Outline each uninfected red blood cell.
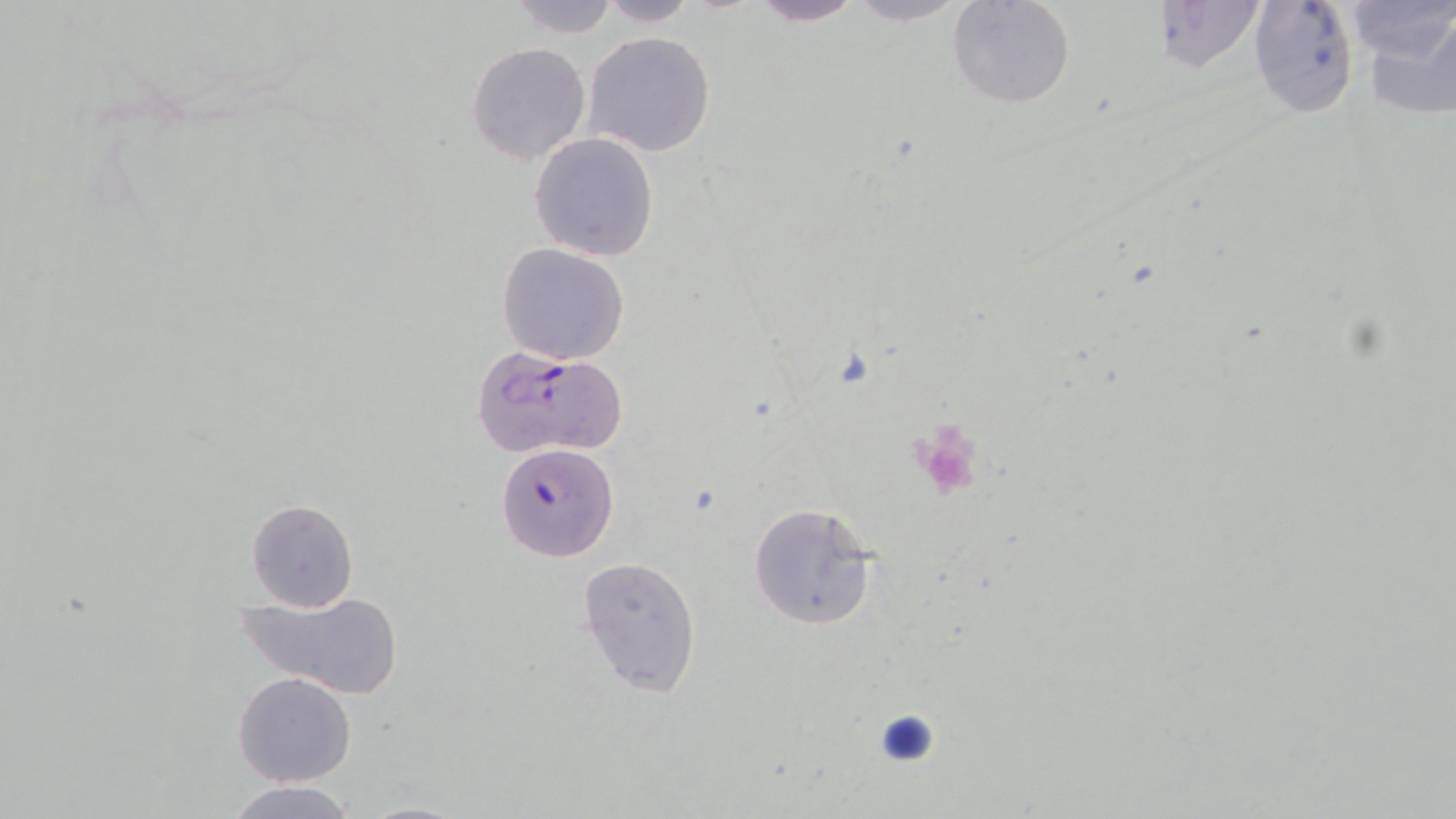

Approximate bounding boxes as (x1,y1)-(x2,y2) corner pairs in pixels.
Uninfected red blood cells: (745,0)-(868,26), (838,0)-(974,26), (946,0)-(1076,110), (1248,0)-(1361,119), (1349,0)-(1456,115), (503,1)-(622,40), (591,1)-(702,26), (1144,3)-(1269,77), (583,30)-(716,156), (466,41)-(591,165), (529,131)-(659,261), (496,242)-(631,365), (246,498)-(359,611), (748,501)-(880,632), (577,556)-(702,697), (234,587)-(405,700), (233,672)-(356,786), (223,780)-(362,818), (354,799)-(472,819).

slide-level diagnosis = Plasmodium falciparum
magnification = 1000x
Plasmodium falciparum-infected red blood cell locations = approximate bounding boxes as (x1,y1)-(x2,y2) corner pairs in pixels: (477,346)-(631,460), (494,443)-(619,562)
modality = light microscopy
platelet locations = approximate bounding boxes as (x1,y1)-(x2,y2) corner pairs in pixels: (910,422)-(984,500)
stain = May-Grünwald-Giemsa
image size = 1456×819 pixels
field of view = one of a larger specimen
preparation = thin blood smear